Identify the parasite.
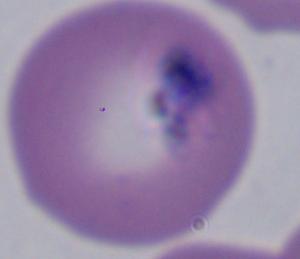
Babesia.

Summary:
  - Modality: photomicrograph
  - Magnification: 1000x